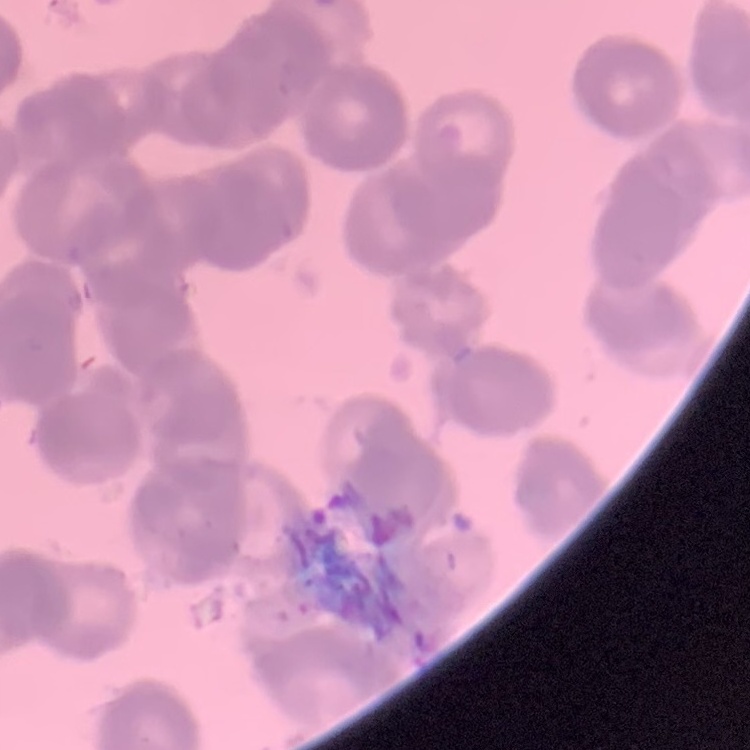

Summary:
  - Red blood cell morphology: rouleaux formation
  - Preparation: thin peripheral smear
  - Stain: Field's or Giemsa
  - Image type: square crop of a larger photomicrograph